Assess this cell for malaria.
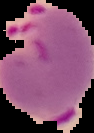

Parasitized.

Summary:
  - Image size: 94×133 pixels
  - Image type: segmented cell region on a black background
  - Preparation: thin blood smear